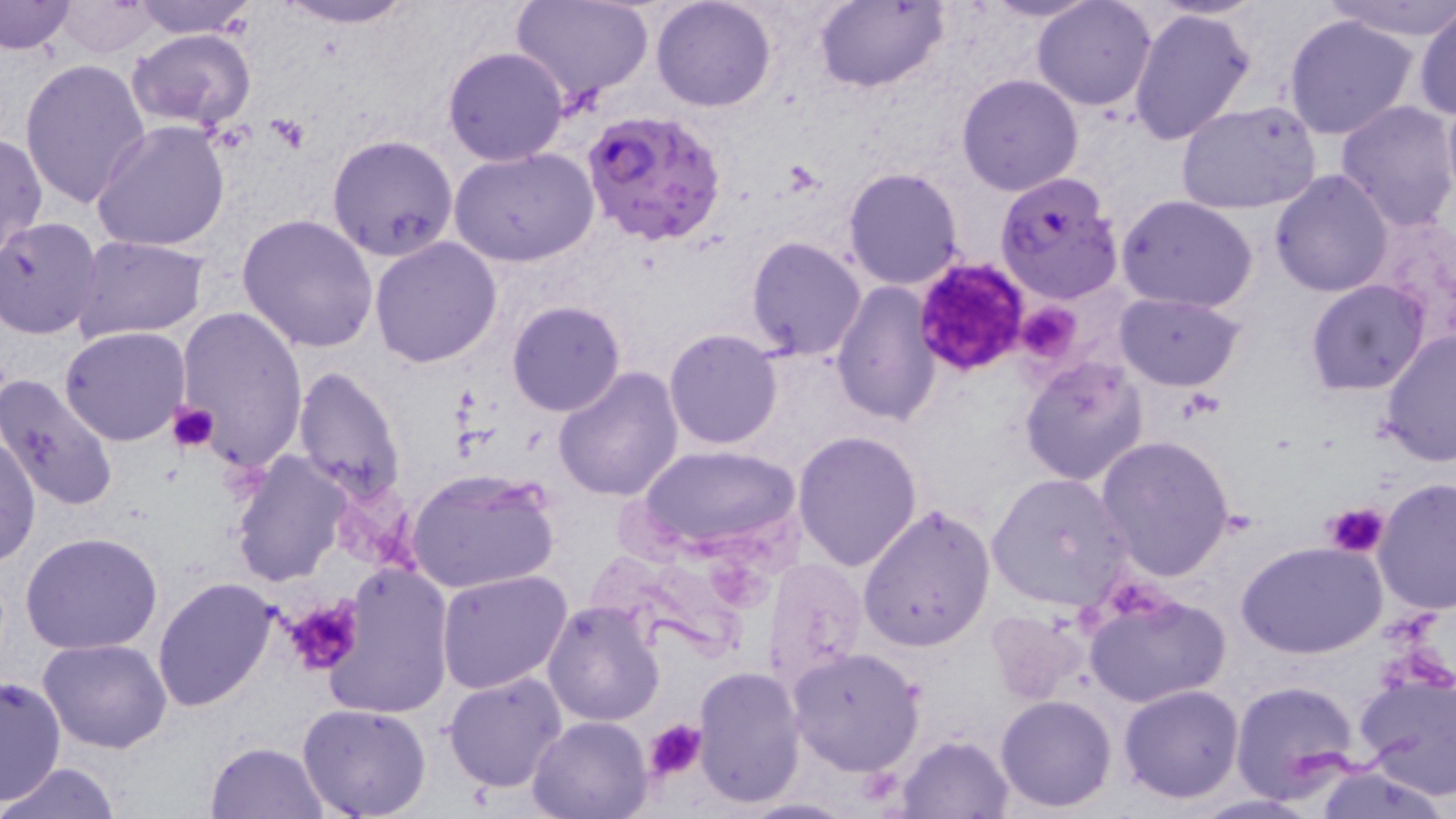
Approximate bounding boxes as [x1, y1, x2, y2] in pixels. Platelet locations: [911, 258, 1030, 377], [1015, 301, 1084, 363], [170, 401, 220, 453], [1323, 503, 1390, 558], [281, 597, 366, 677], [643, 718, 707, 783]. Plasmodium falciparum-infected red blood cell locations: [582, 106, 728, 248], [994, 172, 1123, 304]. Uninfected red blood cell locations: [125, 0, 260, 39], [269, 0, 422, 28], [509, 0, 657, 108], [651, 0, 778, 112], [811, 0, 947, 93], [982, 0, 1098, 23], [1031, 0, 1157, 111], [1326, 0, 1454, 42], [1, 1, 75, 55], [54, 1, 162, 59], [1129, 7, 1256, 147], [1411, 7, 1456, 120], [1281, 12, 1421, 141], [127, 28, 258, 131], [442, 46, 570, 167], [21, 57, 150, 210], [956, 74, 1084, 196], [1441, 88, 1456, 208], [1174, 100, 1323, 216], [1335, 100, 1456, 231], [92, 119, 232, 251], [0, 132, 46, 263], [325, 133, 459, 261], [449, 146, 600, 267], [843, 167, 964, 291], [1269, 169, 1395, 297], [1117, 197, 1259, 313], [1361, 211, 1456, 346], [237, 213, 380, 354], [0, 216, 103, 339], [745, 235, 868, 360], [71, 236, 210, 344], [369, 236, 503, 369], [1305, 279, 1431, 395], [830, 280, 942, 426], [1114, 292, 1246, 391], [506, 301, 628, 418], [175, 307, 308, 471], [60, 326, 191, 446], [664, 327, 784, 448], [1376, 328, 1455, 467], [1019, 357, 1149, 486], [292, 365, 407, 506], [552, 367, 683, 502], [0, 373, 119, 514], [792, 430, 923, 572], [0, 432, 40, 567], [1096, 437, 1237, 582], [636, 446, 800, 551], [229, 452, 350, 585], [406, 466, 560, 596], [986, 473, 1135, 611], [1372, 479, 1456, 614], [858, 502, 995, 652], [19, 531, 163, 655], [1238, 540, 1388, 659], [762, 556, 869, 692], [324, 562, 453, 719], [437, 570, 572, 695], [152, 576, 277, 711], [1082, 589, 1231, 708], [541, 601, 666, 727], [985, 608, 1093, 705], [37, 638, 173, 754], [785, 647, 925, 778], [1353, 663, 1456, 797], [692, 666, 805, 808], [441, 670, 567, 793], [0, 678, 67, 802], [1230, 679, 1362, 802], [1118, 684, 1245, 804], [994, 695, 1118, 813], [298, 703, 432, 819], [528, 714, 653, 817], [898, 734, 1016, 818], [204, 740, 330, 818], [1310, 760, 1451, 819], [3, 761, 122, 818], [735, 796, 859, 817]. Slide-level diagnosis: Plasmodium falciparum. 1000x magnification. Optical microscopy. May-Grünwald-Giemsa-stained preparation. Thin blood smear. Single field of view. Image is 1456×819 pixels.